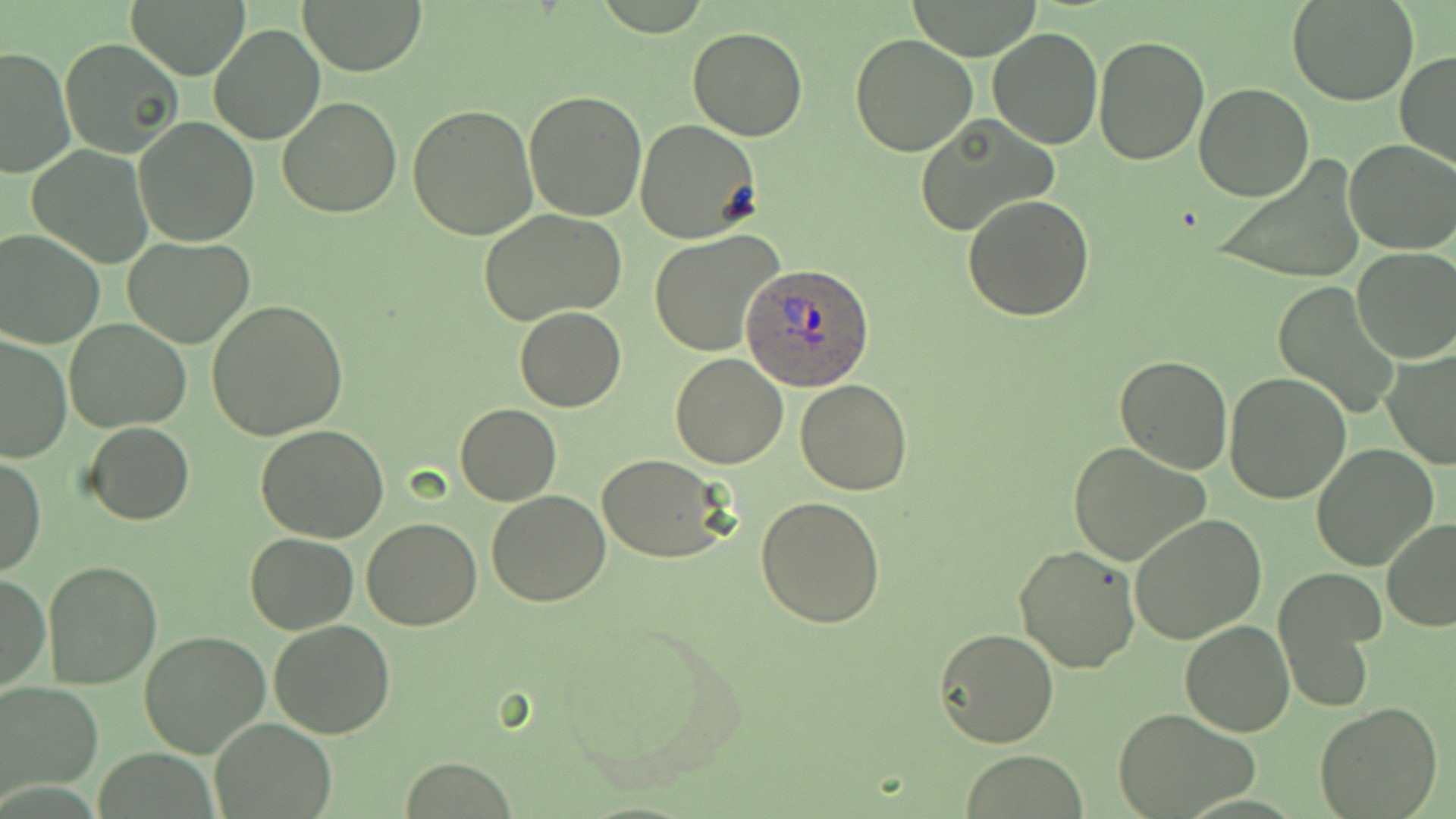
{
  "slide_level_diagnosis": "Plasmodium ovale",
  "modality": "optical microscopy",
  "preparation": "thin blood film",
  "stain": "May-Grünwald-Giemsa",
  "magnification": "1000x",
  "plasmodium_ovale_infected_red_blood_cell_locations": "approximate bounding boxes as (x1,y1)-(x2,y2) corner pairs in pixels: (743,263)-(875,391)",
  "image_size": "1456×819 pixels",
  "field_of_view": "single",
  "uninfected_red_blood_cell_locations": "approximate bounding boxes as (x1,y1)-(x2,y2) corner pairs in pixels: (127,0)-(251,78), (295,0)-(429,75), (1289,0)-(1419,106), (902,2)-(1046,60), (209,23)-(325,146), (687,26)-(807,141), (988,26)-(1103,150), (850,33)-(979,157), (1093,35)-(1208,165), (60,37)-(183,160), (0,46)-(73,178), (1395,50)-(1456,170), (1194,83)-(1314,200), (524,90)-(647,221), (277,97)-(403,219), (408,104)-(539,239), (135,115)-(259,247), (913,115)-(1057,238), (634,119)-(761,241), (1343,140)-(1456,255), (27,147)-(153,266), (1211,155)-(1368,285), (12,184)-(137,330), (962,194)-(1095,322), (479,209)-(630,327), (0,228)-(105,347), (648,230)-(786,356), (124,236)-(255,348), (1353,249)-(1456,364), (1271,282)-(1401,417), (206,300)-(349,441), (515,307)-(626,412), (65,319)-(190,433), (0,333)-(74,463), (1382,348)-(1454,468), (669,352)-(788,469), (1114,356)-(1235,475), (1224,371)-(1350,504), (795,379)-(913,496), (455,403)-(560,505), (84,422)-(194,524), (255,425)-(389,543), (1067,442)-(1211,568), (1312,444)-(1438,571), (1,454)-(45,577), (597,454)-(731,562), (486,491)-(611,607), (757,495)-(888,628), (1130,514)-(1267,646), (361,518)-(481,631), (1381,519)-(1456,632), (247,532)-(357,633), (1013,544)-(1141,674), (42,561)-(161,688), (1273,568)-(1383,713), (0,575)-(50,693), (551,613)-(744,793), (268,619)-(395,738), (1179,620)-(1294,736), (935,628)-(1057,748), (140,630)-(271,757), (0,683)-(102,799), (1314,702)-(1443,819), (1115,708)-(1260,818), (211,717)-(334,818), (960,750)-(1087,818)"
}